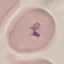

result = malaria parasites detected
stain = Giemsa
capture = smartphone camera at the microscope eyepiece
preparation = thin blood smear
image type = cell patch, automatically extracted from a larger field of view and resized to 64 × 64 pixels